Give the position of every leukocyte visible.
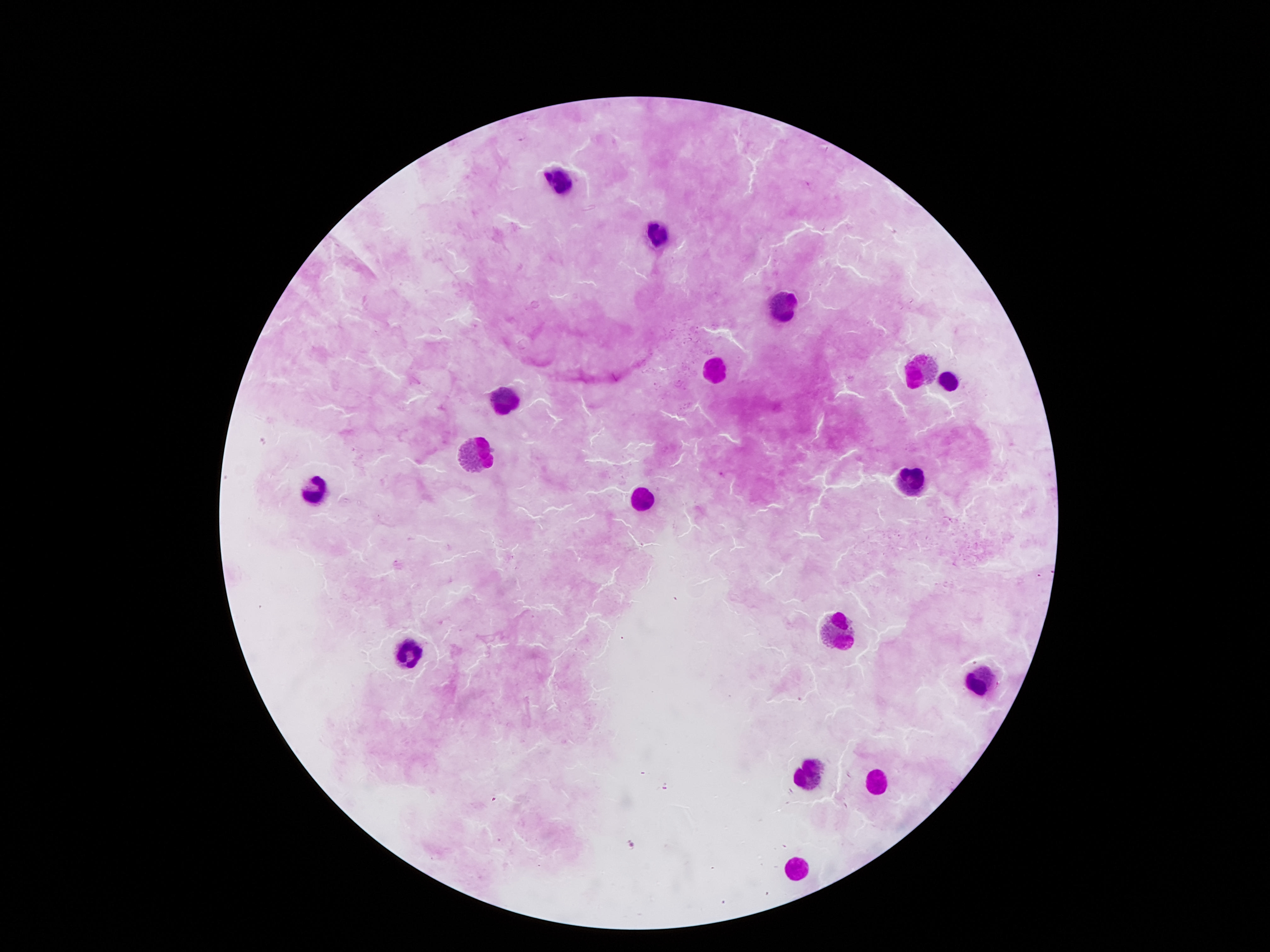
Approximate centers as [x, y] in pixels.
Leukocytes: [560, 180], [658, 238], [779, 307], [711, 370], [916, 371], [948, 384], [501, 392], [477, 460], [912, 482], [312, 491], [641, 500], [834, 633], [407, 649], [981, 684], [805, 772], [879, 780], [799, 864].

image size = 1270×952 pixels
patient malaria status = negative
stain = Giemsa
magnification = 100x
capture = smartphone camera through the microscope eyepiece
field of view = single
preparation = thick peripheral-blood smear